Assess this cell for malaria.
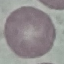
It is uninfected.

Thin blood smear. Cell patch, automatically extracted from a larger field of view and resized to 64 × 64 pixels. Giemsa-stained preparation. Photographed with a smartphone camera at the microscope eyepiece.